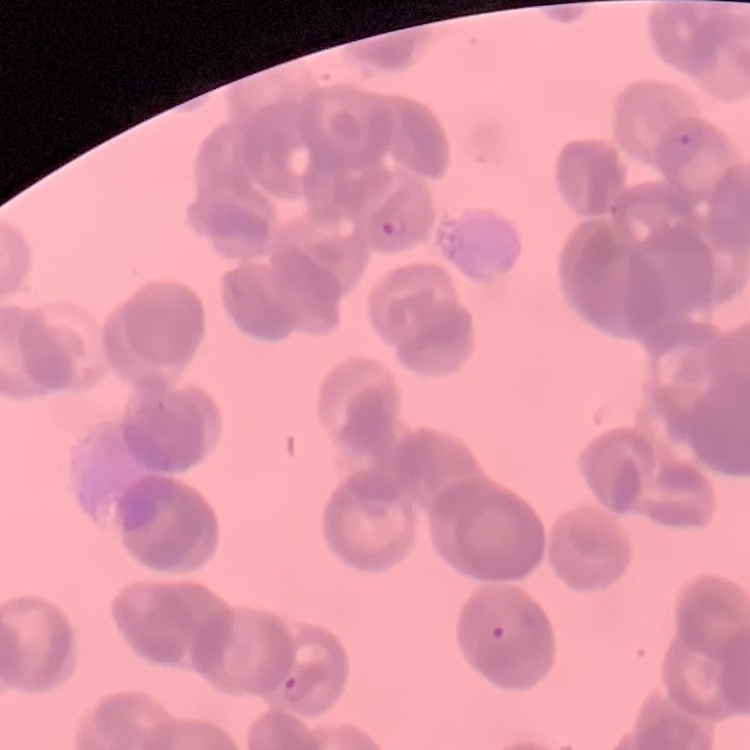

{
  "erythrocyte_morphology": "rouleaux formation",
  "image_type": "one tile cut from a larger photomicrograph",
  "preparation": "thin blood smear",
  "stain": "Field's or Giemsa"
}